Locate every Plasmodium parasite.
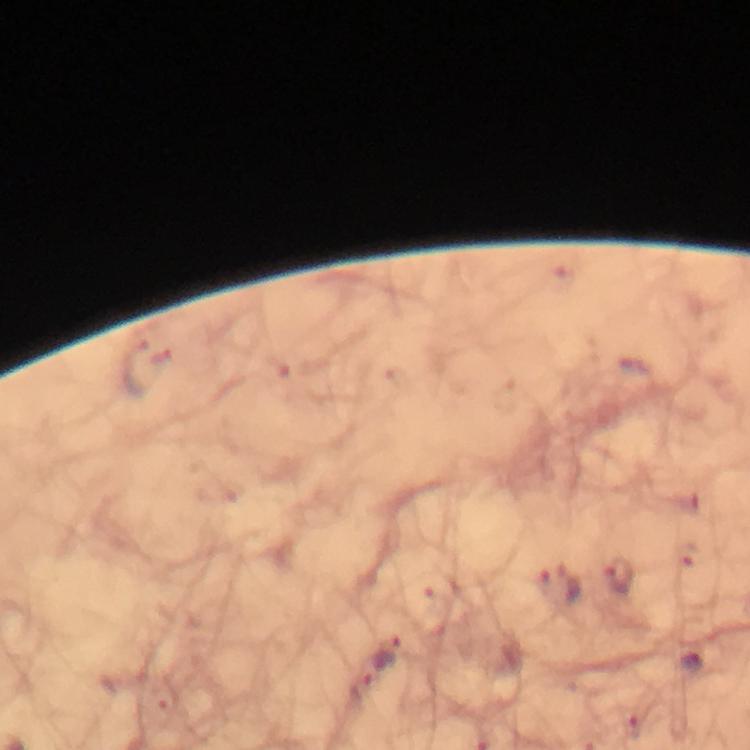

Approximate centers as {x, y} in pixels.
Plasmodium parasites: {620, 577}, {559, 588}, {386, 654}, {692, 664}, {364, 687}.

Summary:
  - Context: from a malaria diagnostic workup
  - Cropped from: one field of view
  - Image size: 750×750 pixels
  - Immersion oil: applied
  - Stain: Giemsa
  - Preparation: thick smear
  - Magnification: 100x
  - Capture: smartphone photograph through a microscope